Classify this cell by malaria status.
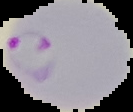
It is parasitized.

From a thin blood smear. Image is 133×112 pixels. Segmented cell region on a black background.